Assess this cell for malaria.
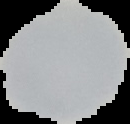

Uninfected.

Summary:
  - Image type: segmented cell region on a black background
  - Preparation: thin blood smear
  - Image size: 130×124 pixels